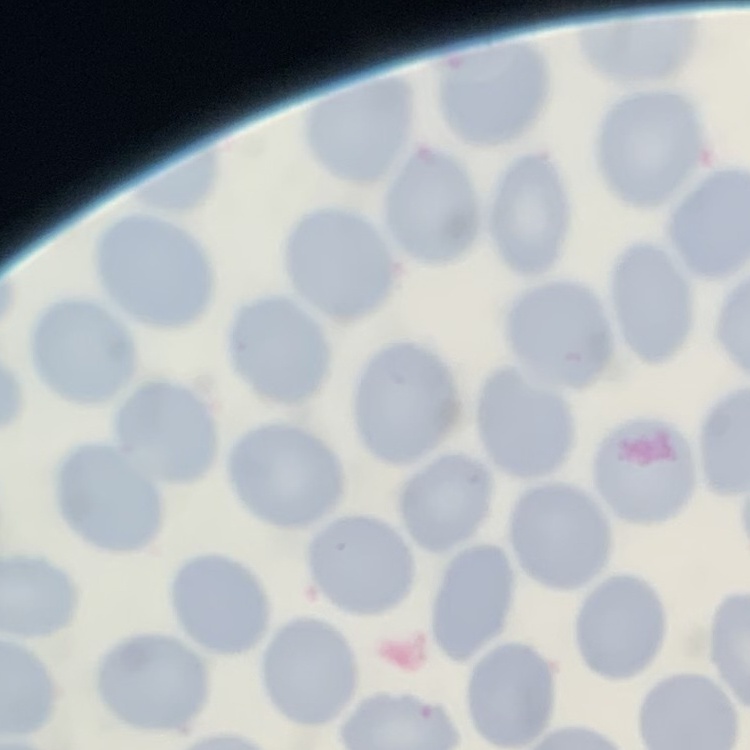
red blood cell morphology = no rouleaux formation
image type = one tile cut from a larger photomicrograph
stain = Field's or Giemsa
preparation = thin peripheral smear